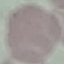

Summary:
  - Result: no malaria parasites seen
  - Stain: Giemsa
  - Image type: cell patch, automatically extracted from a larger field of view and resized to 64 × 64 pixels
  - Capture: smartphone camera at the microscope eyepiece
  - Preparation: thin smear